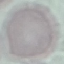
Result: no malaria parasites seen. Automatically extracted cell patch, resized to 64 × 64 pixels. Thin smear of blood. Acquired by smartphone through the microscope eyepiece. Giemsa-stained preparation.